Identify the preparation type.
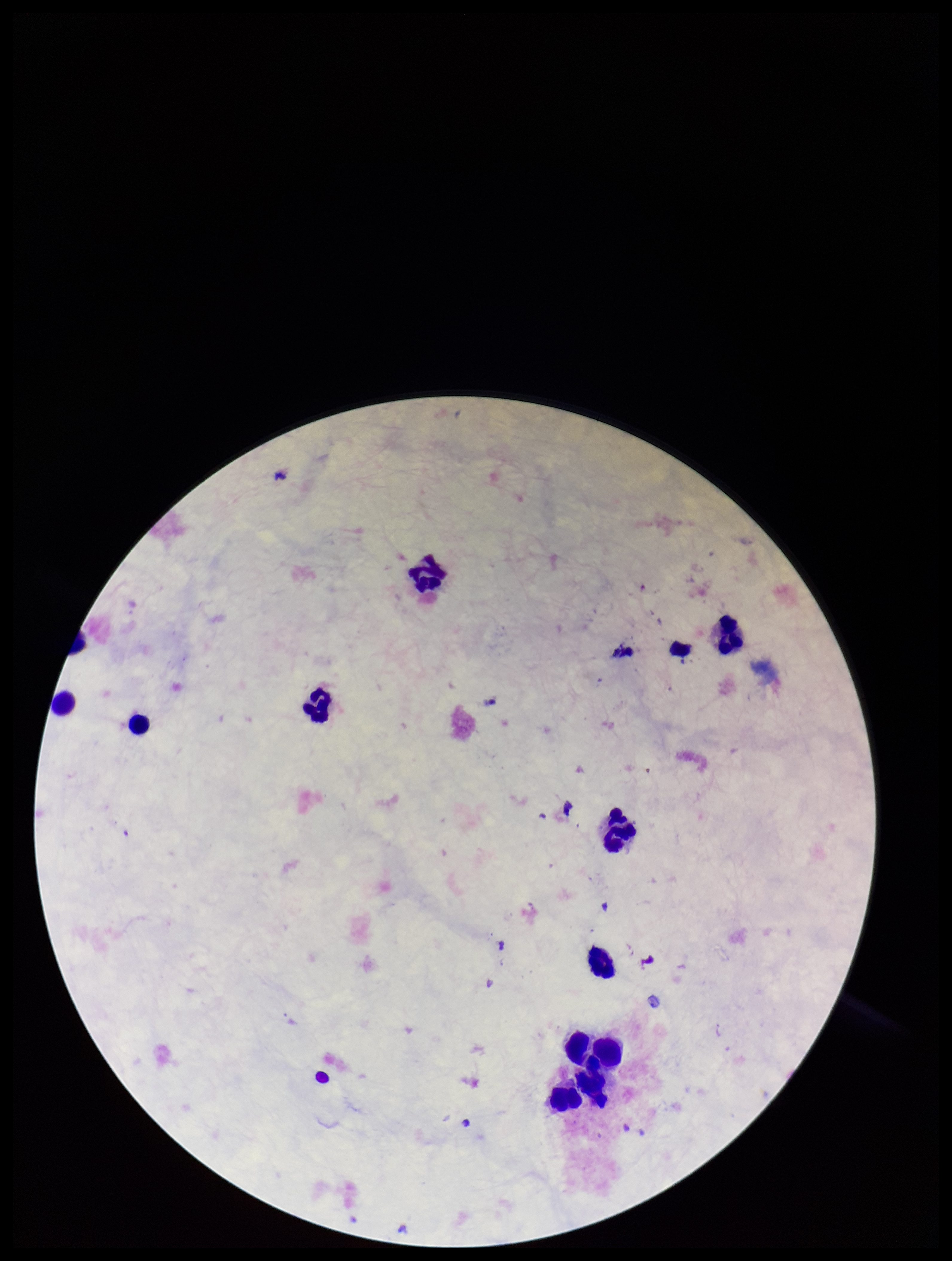

It is a thick blood smear.

Plasmodium parasites: none seen. Image is 952×1261 pixels. Smartphone photograph taken through the eyepiece of a microscope. Patient malaria status: negative. Parasite count: 0. Stained with Giemsa. One field from this slide. Leukocyte count: 11.